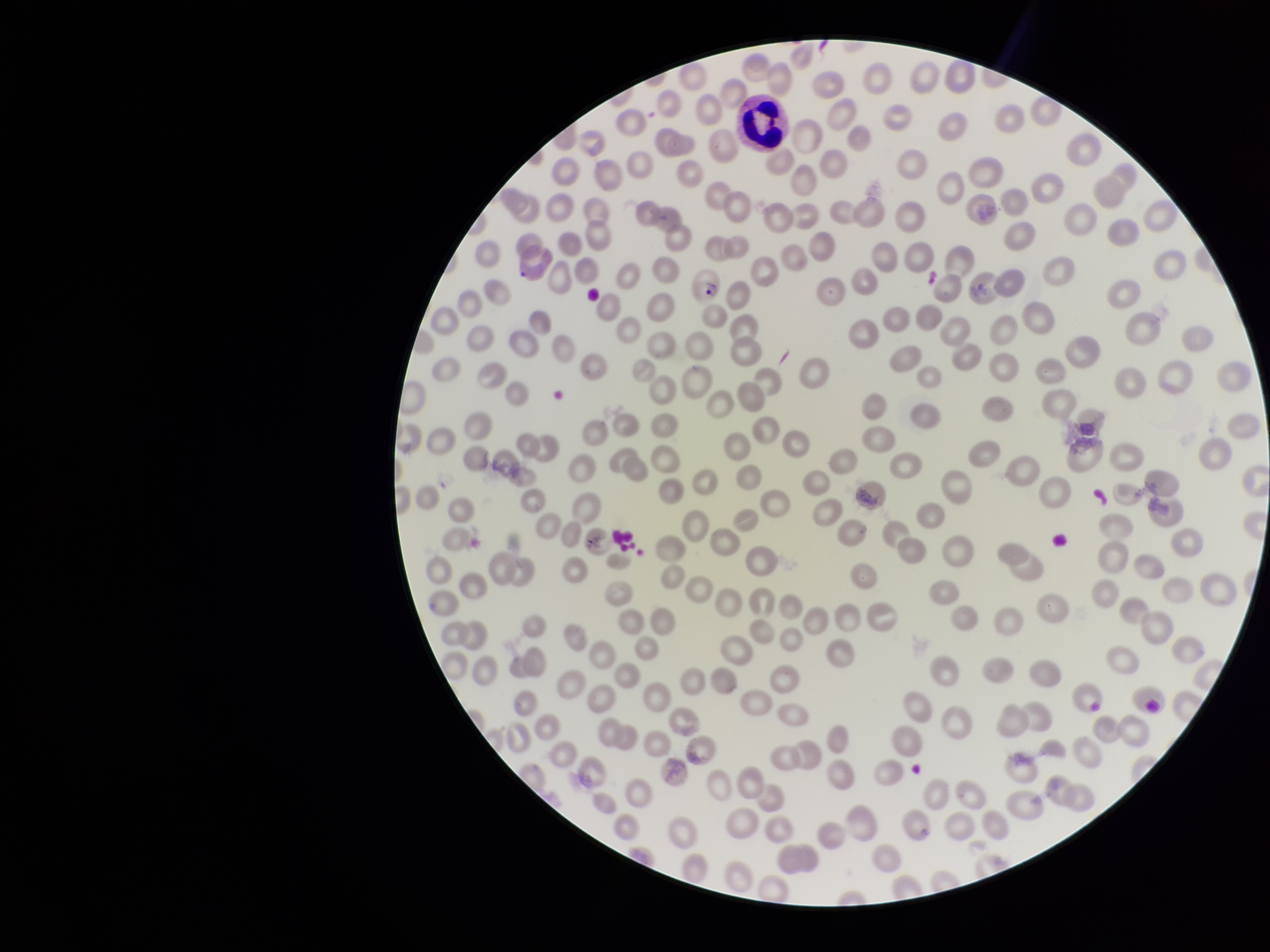
{
  "parasitized_red_blood_cell_count": 3,
  "patient_malaria_status": "infected",
  "image_size": "1270×952 pixels",
  "field_of_view": "one from this slide",
  "stain": "Giemsa",
  "species_reported_for_this_patient": "Plasmodium vivax",
  "capture": "smartphone photograph through the microscope eyepiece",
  "preparation": "thin",
  "parasitized_red_blood_cells": "seen",
  "red_blood_cell_count": 251
}